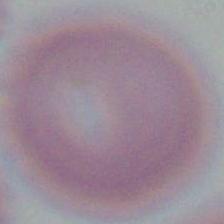
Summary:
  - Identification: red blood cell
  - Modality: micrograph
  - Magnification: 1000x